Outline each blood parasite and name the species.
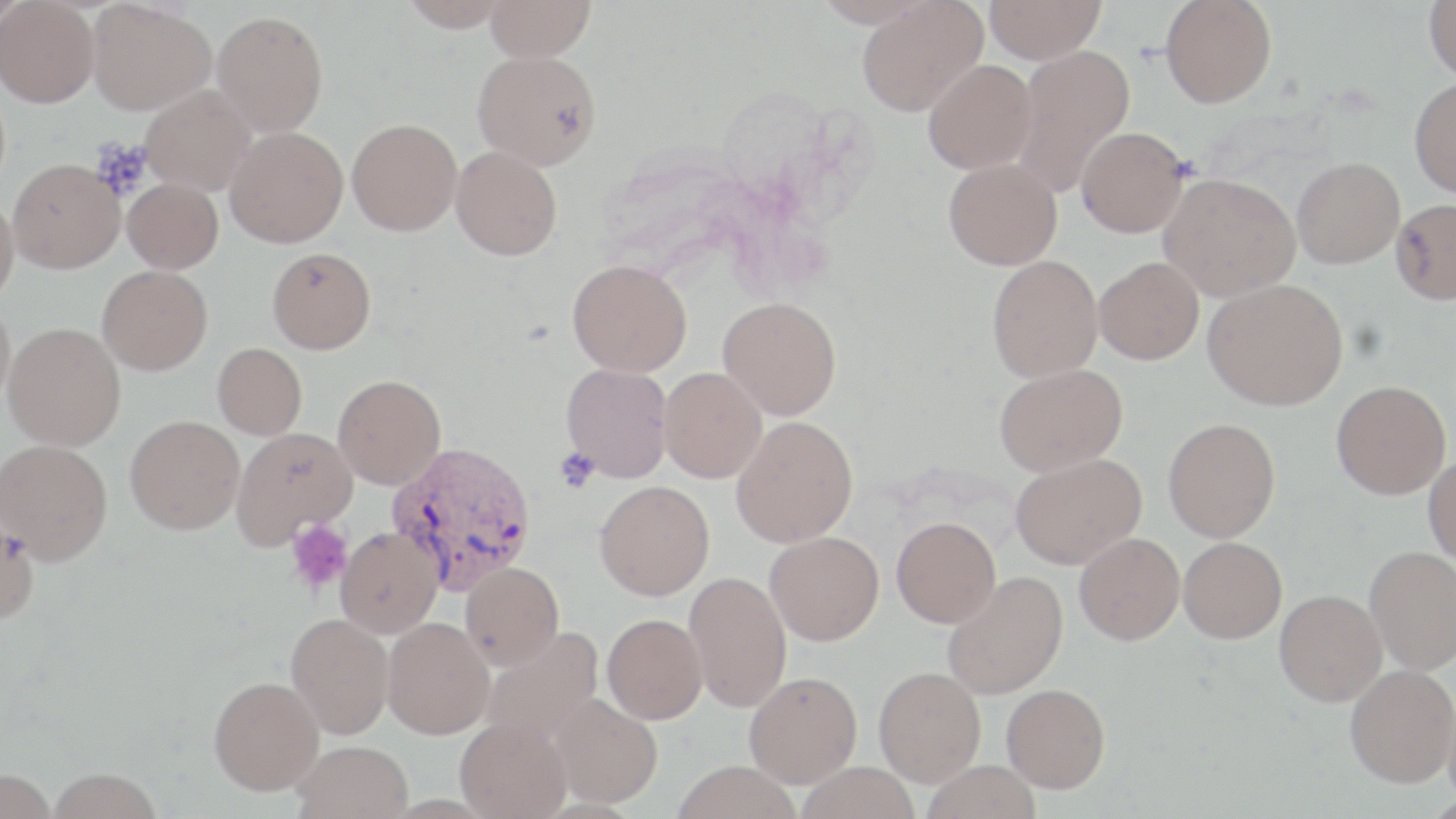
Approximate bounding boxes as named x1/y1/x2/y2 corners in pixels.
Plasmodium vivax-infected red blood cells: (x1=386, y1=441, x2=537, y2=594).
No Plasmodium falciparum, Plasmodium ovale, Plasmodium malariae, Babesia divergens, or Trypanosoma brucei observed.

Summary:
  - Platelet locations: (x1=556, y1=449, x2=598, y2=492), (x1=285, y1=520, x2=354, y2=593)
  - Uninfected red blood cell locations: (x1=0, y1=0, x2=29, y2=34), (x1=86, y1=0, x2=215, y2=115), (x1=397, y1=0, x2=513, y2=31), (x1=484, y1=0, x2=596, y2=61), (x1=815, y1=0, x2=933, y2=28), (x1=984, y1=0, x2=1105, y2=64), (x1=1423, y1=0, x2=1456, y2=83), (x1=856, y1=1, x2=987, y2=116), (x1=1160, y1=1, x2=1277, y2=108), (x1=0, y1=2, x2=99, y2=107), (x1=212, y1=10, x2=328, y2=138), (x1=1012, y1=44, x2=1136, y2=197), (x1=472, y1=50, x2=601, y2=170), (x1=923, y1=59, x2=1037, y2=174), (x1=1409, y1=77, x2=1456, y2=198), (x1=141, y1=85, x2=256, y2=195), (x1=347, y1=118, x2=462, y2=235), (x1=1076, y1=126, x2=1189, y2=238), (x1=225, y1=127, x2=348, y2=248), (x1=451, y1=146, x2=562, y2=260), (x1=1292, y1=157, x2=1404, y2=268), (x1=943, y1=158, x2=1062, y2=270), (x1=8, y1=159, x2=124, y2=273), (x1=1159, y1=173, x2=1301, y2=301), (x1=123, y1=178, x2=223, y2=274), (x1=0, y1=195, x2=19, y2=307), (x1=1390, y1=198, x2=1455, y2=303), (x1=267, y1=247, x2=376, y2=354), (x1=987, y1=255, x2=1103, y2=382), (x1=1094, y1=256, x2=1204, y2=364), (x1=567, y1=259, x2=692, y2=376), (x1=97, y1=265, x2=212, y2=375), (x1=1203, y1=278, x2=1348, y2=410), (x1=718, y1=297, x2=841, y2=420), (x1=0, y1=300, x2=15, y2=412), (x1=2, y1=322, x2=126, y2=451), (x1=212, y1=343, x2=307, y2=440), (x1=560, y1=363, x2=674, y2=483), (x1=994, y1=363, x2=1128, y2=476), (x1=658, y1=367, x2=767, y2=483), (x1=333, y1=374, x2=446, y2=489), (x1=1331, y1=381, x2=1451, y2=499), (x1=125, y1=415, x2=245, y2=535), (x1=731, y1=416, x2=858, y2=548), (x1=1163, y1=418, x2=1280, y2=542), (x1=231, y1=427, x2=357, y2=549), (x1=0, y1=439, x2=112, y2=565), (x1=1011, y1=452, x2=1146, y2=569), (x1=1423, y1=457, x2=1456, y2=569), (x1=594, y1=480, x2=715, y2=600), (x1=0, y1=512, x2=39, y2=626), (x1=891, y1=516, x2=1001, y2=628), (x1=336, y1=527, x2=443, y2=638), (x1=765, y1=531, x2=884, y2=645), (x1=1074, y1=532, x2=1185, y2=645), (x1=1178, y1=537, x2=1287, y2=643), (x1=1365, y1=546, x2=1456, y2=674), (x1=460, y1=562, x2=564, y2=669), (x1=684, y1=571, x2=791, y2=712), (x1=942, y1=571, x2=1068, y2=699), (x1=1275, y1=589, x2=1387, y2=706), (x1=286, y1=614, x2=394, y2=739), (x1=602, y1=614, x2=707, y2=724), (x1=382, y1=617, x2=495, y2=739), (x1=481, y1=627, x2=604, y2=746), (x1=1345, y1=664, x2=1456, y2=787), (x1=874, y1=666, x2=986, y2=786), (x1=744, y1=671, x2=862, y2=787), (x1=209, y1=676, x2=324, y2=795), (x1=1001, y1=683, x2=1110, y2=793), (x1=1443, y1=688, x2=1456, y2=809), (x1=549, y1=692, x2=662, y2=808), (x1=456, y1=717, x2=572, y2=818), (x1=292, y1=740, x2=413, y2=819), (x1=921, y1=759, x2=1042, y2=819), (x1=672, y1=760, x2=801, y2=819), (x1=796, y1=761, x2=921, y2=819), (x1=48, y1=768, x2=163, y2=819), (x1=0, y1=769, x2=58, y2=819)
  - Slide-level diagnosis: Plasmodium vivax
  - Magnification: 1000x
  - Stain: May-Grünwald-Giemsa
  - Modality: light microscopy
  - Image size: 1456×819 pixels
  - Preparation: thin blood smear
  - Field of view: single